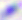

Captured at 400x magnification. Toxoplasma gondii is seen. Photomicrograph.